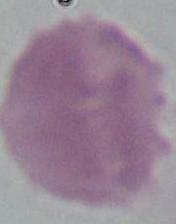

Summary:
  - Identification: erythrocyte
  - Modality: photomicrograph
  - Magnification: 1000x